Assess for malaria.
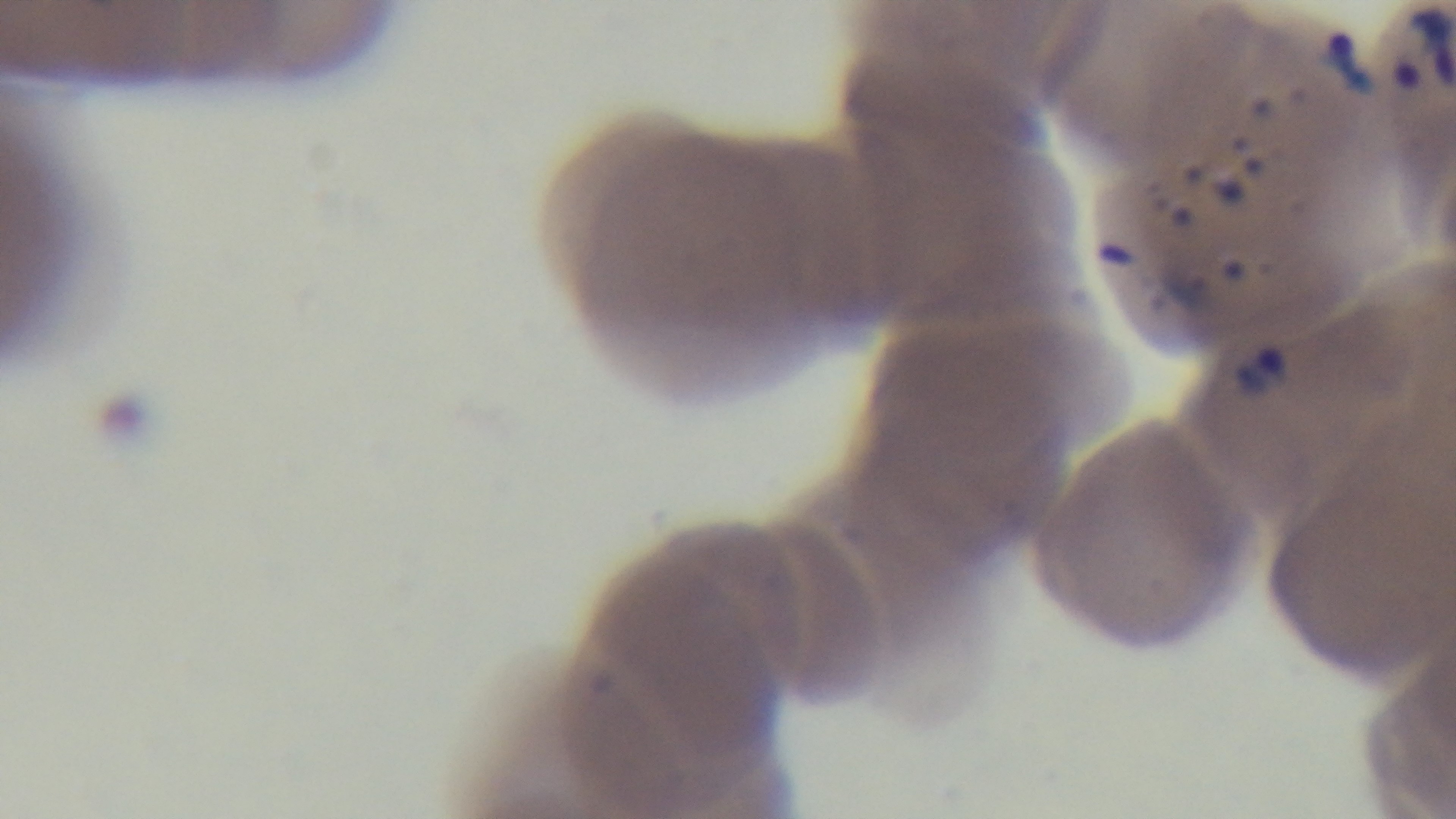

Positive.

Summary:
  - Objective: 100x oil immersion
  - Capture: mounted 4K digital camera
  - Modality: light microscopy
  - Preparation: thin smear
  - Field of view: single
  - Stain: Giemsa